Classify this cell by malaria status.
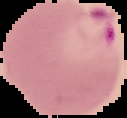
It is parasitized.

image type = segmented cell region with the area outside set to black
preparation = thin blood film
image size = 127×118 pixels